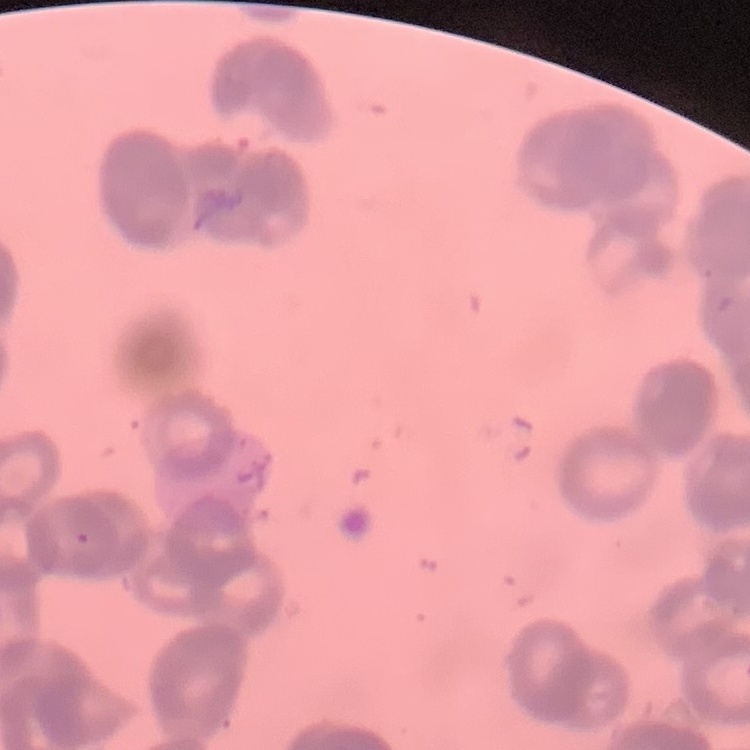
Summary:
  - Red blood cell morphology: rouleaux formation
  - Stain: Field's or Giemsa
  - Image type: square crop of a larger photomicrograph
  - Preparation: thin blood film